Identify the parasite.
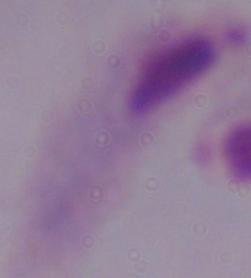
A trichomonad.

Micrograph. 1000x magnification.